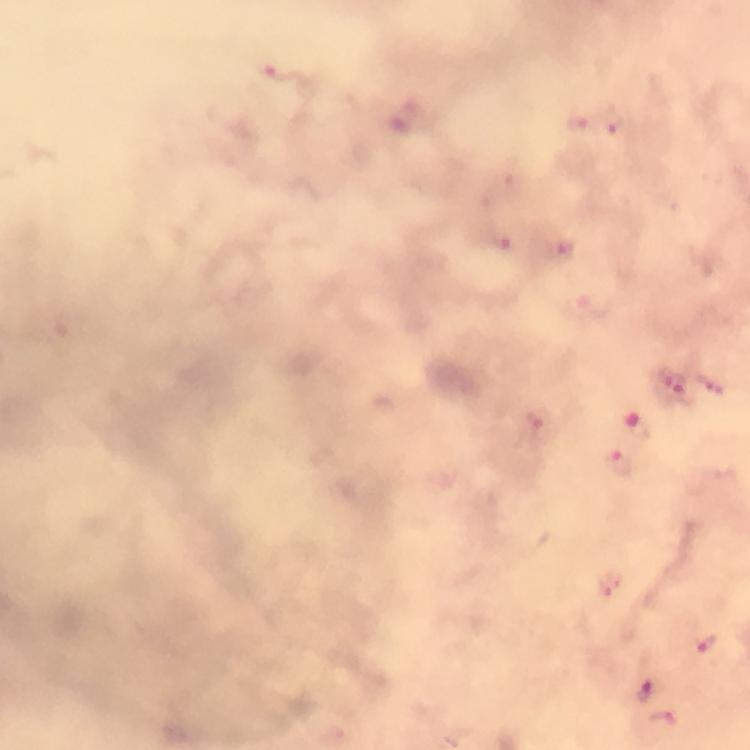

Plasmodium parasite locations = approximate object centers, in pixels from the top-left corner: (x=279, y=71), (x=613, y=120), (x=579, y=122), (x=496, y=241), (x=563, y=250), (x=675, y=383), (x=711, y=385), (x=538, y=419), (x=640, y=427), (x=621, y=461), (x=611, y=584), (x=706, y=646), (x=645, y=690), (x=662, y=720)
magnification = 100x
image size = 750×750 pixels
stain = Giemsa
capture = smartphone camera through the microscope
context = from a diagnostic examination for malaria
preparation = thick blood film
immersion oil = applied
cropped from = one field of view